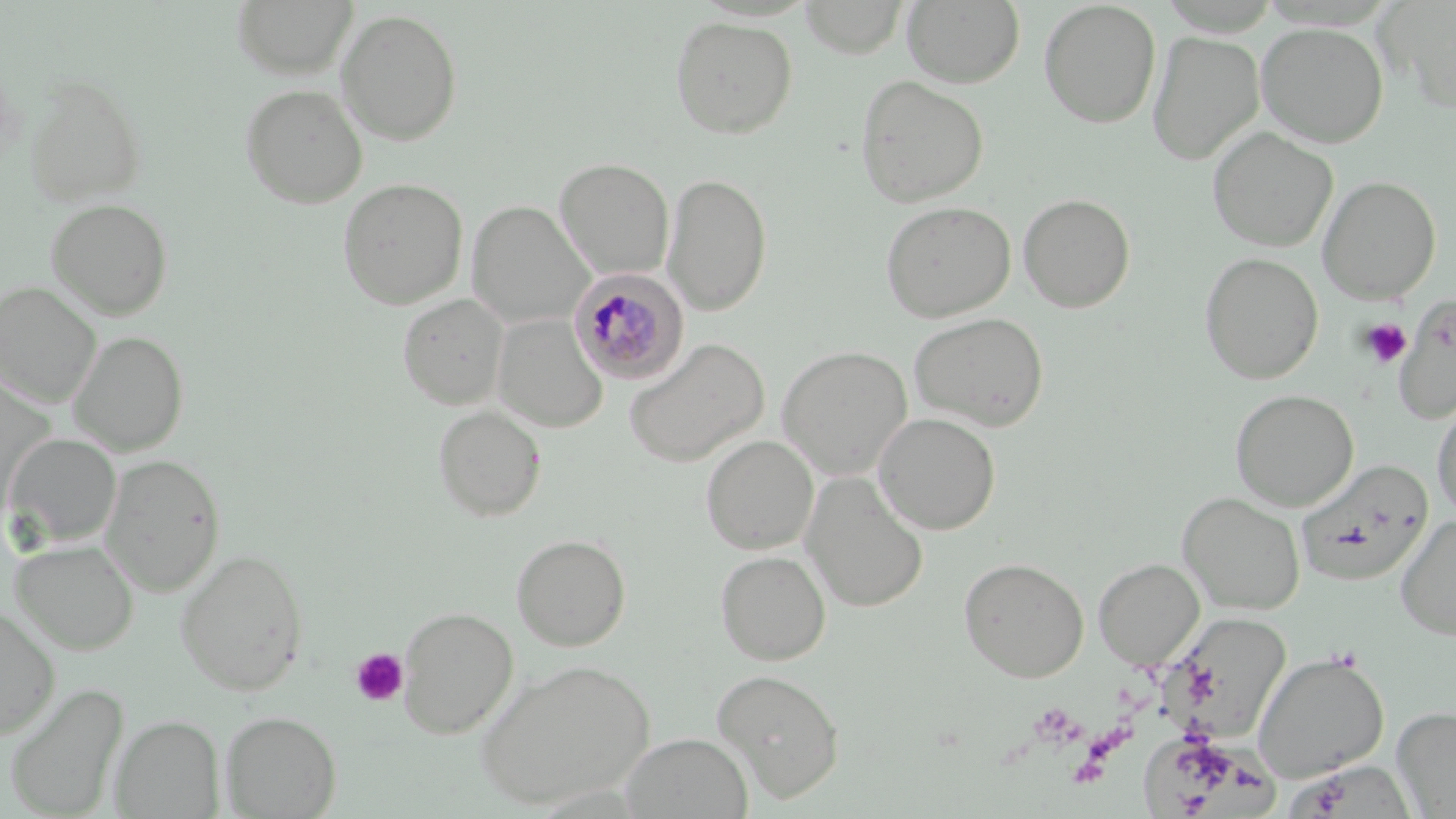
Summary:
  - Coordinate format: approximate bounding boxes as (x1,y1)-(x2,y2) corner pairs in pixels
  - Platelet locations: (1359,318)-(1412,369), (350,647)-(409,707)
  - Plasmodium malariae-infected red blood cell locations: (568,269)-(688,384)
  - Uninfected red blood cell locations: (231,0)-(357,80), (901,0)-(1025,89), (798,1)-(909,58), (1038,1)-(1161,128), (1382,1)-(1456,114), (336,9)-(463,146), (669,15)-(798,139), (1256,22)-(1389,148), (1147,30)-(1265,166), (855,74)-(989,208), (26,78)-(146,206), (239,83)-(368,209), (1207,127)-(1337,252), (555,158)-(674,279), (663,172)-(773,316), (1318,175)-(1441,304), (337,178)-(468,309), (1017,193)-(1136,313), (46,198)-(173,320), (880,200)-(1016,322), (466,201)-(593,328), (1199,252)-(1323,384), (1,281)-(101,407), (397,293)-(509,410), (1393,295)-(1456,424), (908,312)-(1050,430), (492,314)-(607,433), (69,331)-(188,456), (623,338)-(769,468), (777,345)-(913,480), (1230,389)-(1358,511), (1431,397)-(1456,521), (432,405)-(547,522), (873,412)-(1000,535), (5,433)-(121,547), (700,435)-(819,554), (100,453)-(225,597), (1296,458)-(1434,587), (800,473)-(928,613), (1177,492)-(1305,615), (1395,515)-(1456,640), (510,533)-(631,652), (10,539)-(139,655), (174,548)-(309,696), (715,550)-(831,666), (959,557)-(1089,682), (1093,559)-(1204,668), (0,604)-(60,739), (397,606)-(519,739), (1171,614)-(1292,743), (1252,651)-(1389,784), (475,659)-(654,810), (711,668)-(845,801), (3,681)-(129,818), (1392,706)-(1456,817), (220,711)-(341,818), (111,715)-(224,817), (620,733)-(753,819)
  - Slide-level diagnosis: Plasmodium malariae
  - Preparation: thin blood smear
  - Modality: optical microscopy
  - Magnification: 1000x
  - Image size: 1456×819 pixels
  - Stain: May-Grünwald-Giemsa
  - Field of view: single